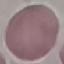

malaria_status: uninfected
preparation: thin smear
capture: smartphone camera at the microscope eyepiece
image_type: automatically extracted cell patch, resized to 64 × 64 pixels
stain: Giemsa